Mark where leukocytes are.
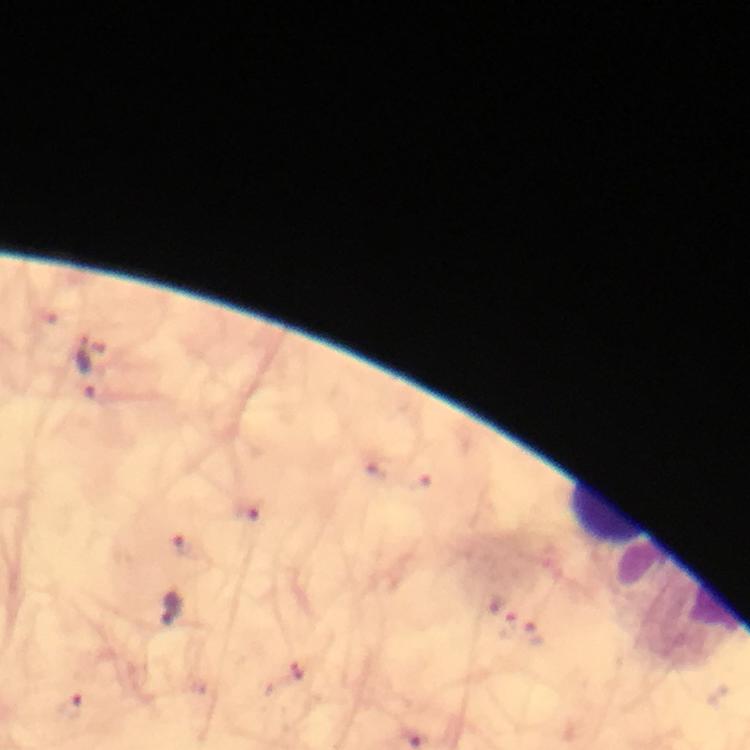
Approximate object centers, in pixels from the top-left corner.
Leukocytes: (x=607, y=511).

stain: Giemsa
image_size: 750×750 pixels
capture: smartphone camera through the microscope
magnification: 100x
cropped_from: a single field of view
context: from a malaria diagnostic workup
immersion_oil: applied
malaria_parasite_locations: 'approximate object centers, in pixels from the top-left corner: (x=90, y=365), (x=248, y=512), (x=186, y=545), (x=172, y=608), (x=507, y=625), (x=534, y=635), (x=297, y=669), (x=68, y=704)'
preparation: thick smear